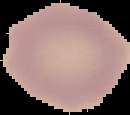

Summary:
  - Image type: segmented cell region with the area outside set to black
  - Malaria status: uninfected
  - Preparation: thin blood smear
  - Image size: 130×115 pixels